Mark where leukocytes are.
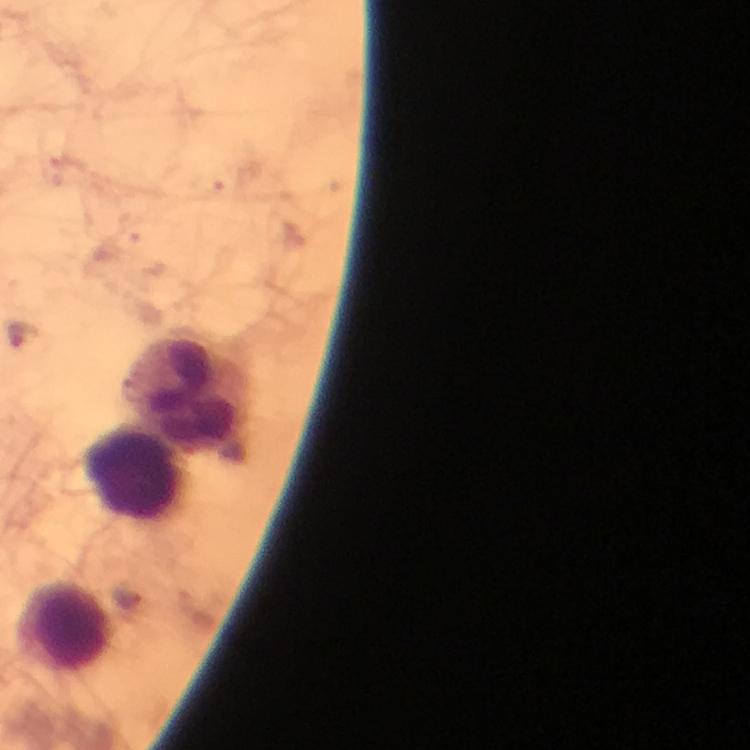
Approximate object centers, in pixels from the top-left corner.
Leukocytes: (x=192, y=399), (x=136, y=475), (x=66, y=627).

cropped from = a single field of view
immersion oil = used
capture = smartphone camera through the microscope
stain = Giemsa
preparation = thick blood film
magnification = 100x
malaria parasites = none detected
context = from a diagnostic examination for malaria
image size = 750×750 pixels